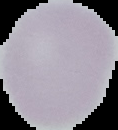

{
  "malaria_status": "uninfected",
  "image_size": "118×130 pixels",
  "preparation": "thin blood smear",
  "image_type": "segmented cell region with the area outside set to black"
}